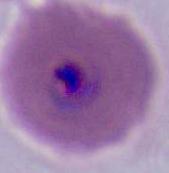
400x or 1000x magnification. A Plasmodium parasite is seen. Micrograph.